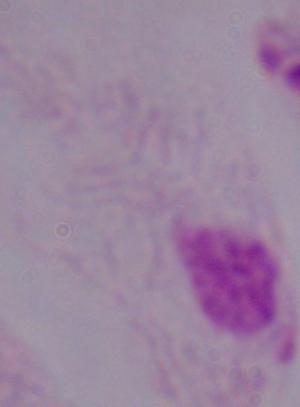
1000x magnification. A trichomonad is shown. Micrograph.